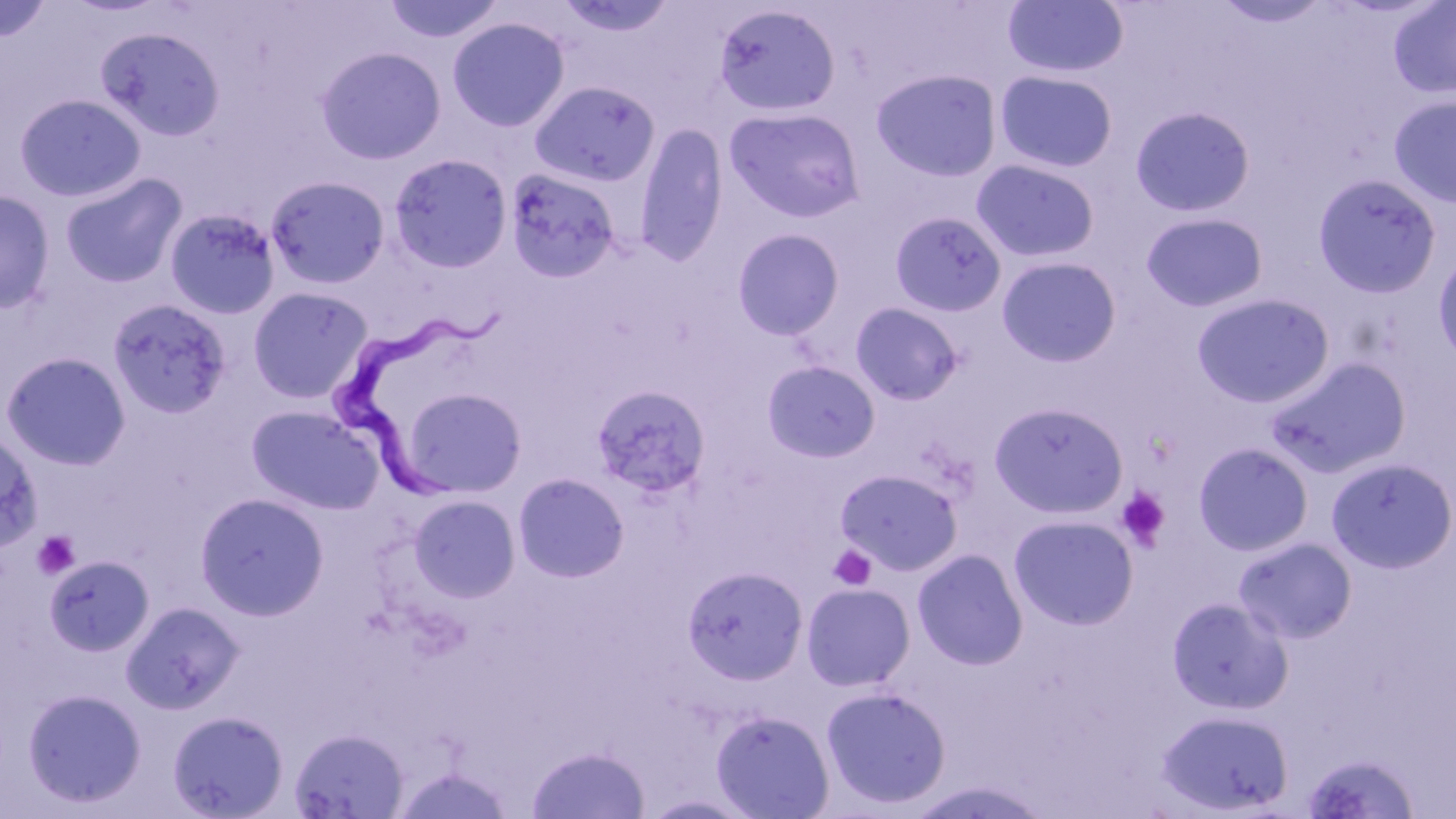

Summary:
  - Coordinate format: approximate bounding boxes as [x1, y1, x2, y2] in pixels
  - Uninfected red blood cell locations: [382, 0, 506, 45], [555, 0, 678, 37], [1002, 0, 1130, 79], [1212, 0, 1333, 28], [0, 1, 53, 42], [1388, 1, 1456, 100], [713, 3, 842, 118], [447, 17, 570, 132], [95, 26, 225, 141], [315, 46, 446, 164], [871, 69, 1002, 182], [995, 70, 1118, 173], [529, 80, 659, 188], [14, 94, 145, 202], [1388, 95, 1456, 208], [724, 106, 865, 223], [1130, 106, 1255, 217], [634, 123, 729, 266], [388, 153, 513, 273], [971, 158, 1100, 262], [505, 168, 623, 282], [60, 172, 186, 288], [1313, 173, 1441, 297], [265, 175, 391, 289], [0, 189, 55, 315], [163, 208, 281, 320], [890, 211, 1007, 317], [1141, 212, 1268, 313], [731, 228, 845, 340], [1433, 251, 1456, 370], [997, 256, 1121, 367], [248, 286, 373, 403], [1192, 292, 1334, 408], [107, 298, 233, 419], [851, 301, 964, 404], [0, 351, 132, 470], [1266, 356, 1411, 478], [762, 360, 880, 463], [591, 383, 711, 500], [400, 387, 526, 498], [989, 402, 1128, 519], [246, 404, 383, 515], [0, 429, 43, 553], [1193, 441, 1314, 556], [1325, 457, 1456, 574], [835, 468, 963, 575], [512, 472, 631, 583], [194, 492, 330, 621], [408, 494, 521, 602], [1008, 514, 1139, 631], [1233, 536, 1358, 644], [913, 549, 1029, 669], [44, 555, 154, 657], [682, 565, 809, 684], [801, 582, 915, 691], [1167, 596, 1292, 714], [121, 600, 244, 714], [821, 686, 951, 810], [22, 688, 147, 808], [711, 709, 834, 818], [167, 710, 289, 819], [1156, 710, 1294, 815], [290, 727, 409, 819], [527, 744, 650, 818], [1301, 751, 1421, 818]
  - Trypanosoma brucei locations: [332, 298, 517, 510]
  - Platelet locations: [1115, 486, 1171, 551], [32, 531, 79, 580], [828, 544, 877, 591]
  - Slide-level diagnosis: Trypanosoma brucei
  - Stain: May-Grünwald-Giemsa
  - Image size: 1456×819 pixels
  - Preparation: thin blood film
  - Field of view: one of a larger specimen
  - Modality: optical microscopy
  - Magnification: 1000x